Draw a bounding box around every leukocyte (white blood cell).
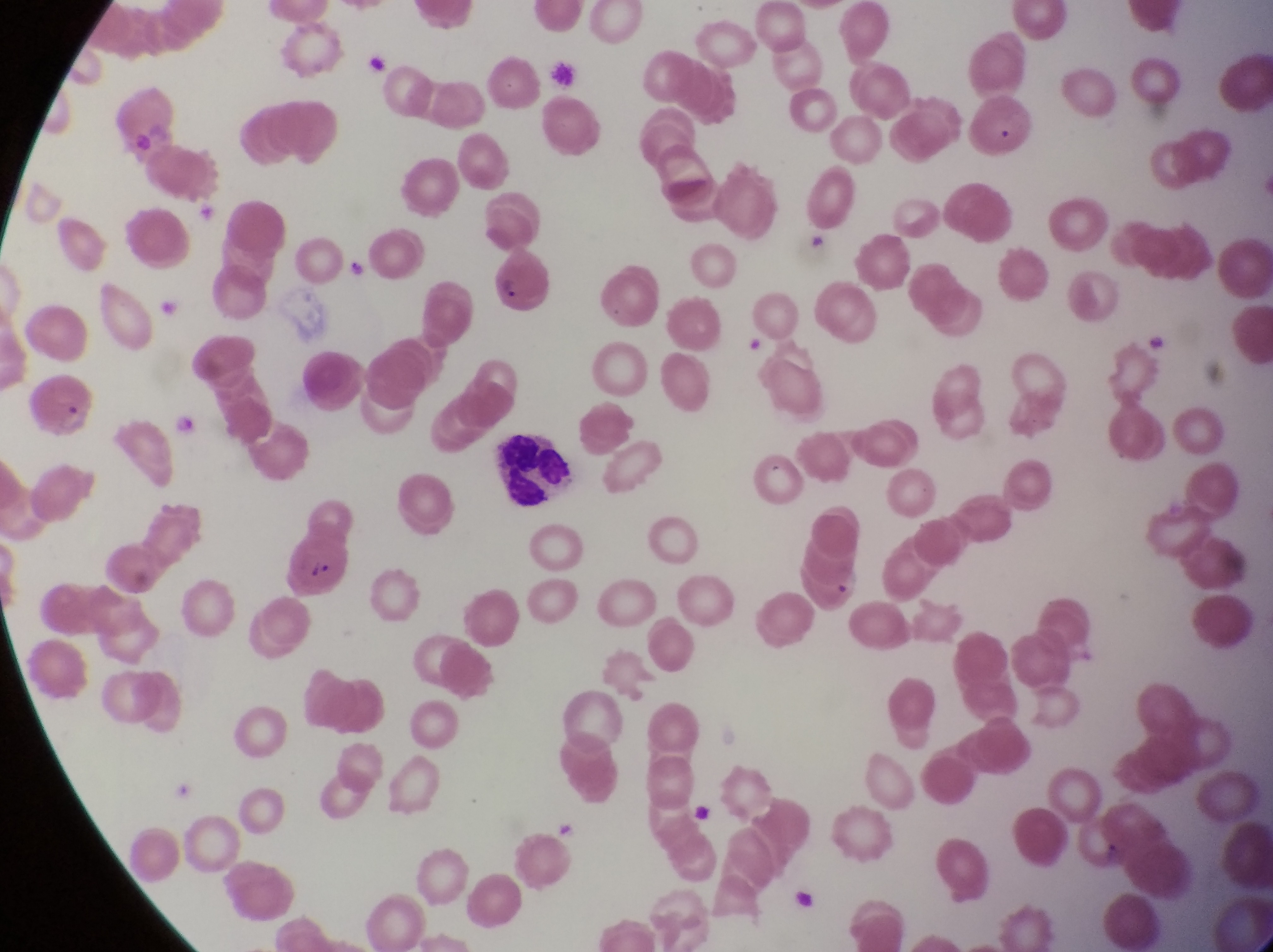
Approximate bounding boxes as (left, top, right, bottom) in pixels.
Leukocytes: (495, 427, 592, 522).

Summary:
  - Artifact (platelet-like body, stain precipitate, or debris) locations: (687, 804, 720, 829)
  - Parasitised red blood cell locations: (285, 529, 357, 601)
  - Trophozoite locations: (335, 247, 375, 289), (167, 410, 202, 440)
  - Preparation: thin blood film
  - Magnification: 1000x
  - Field of view: single
  - Image size: 1273×952 pixels
  - Capture: smartphone photograph through the eyepiece of an Olympus CX-23 microscope
  - Country: Uganda